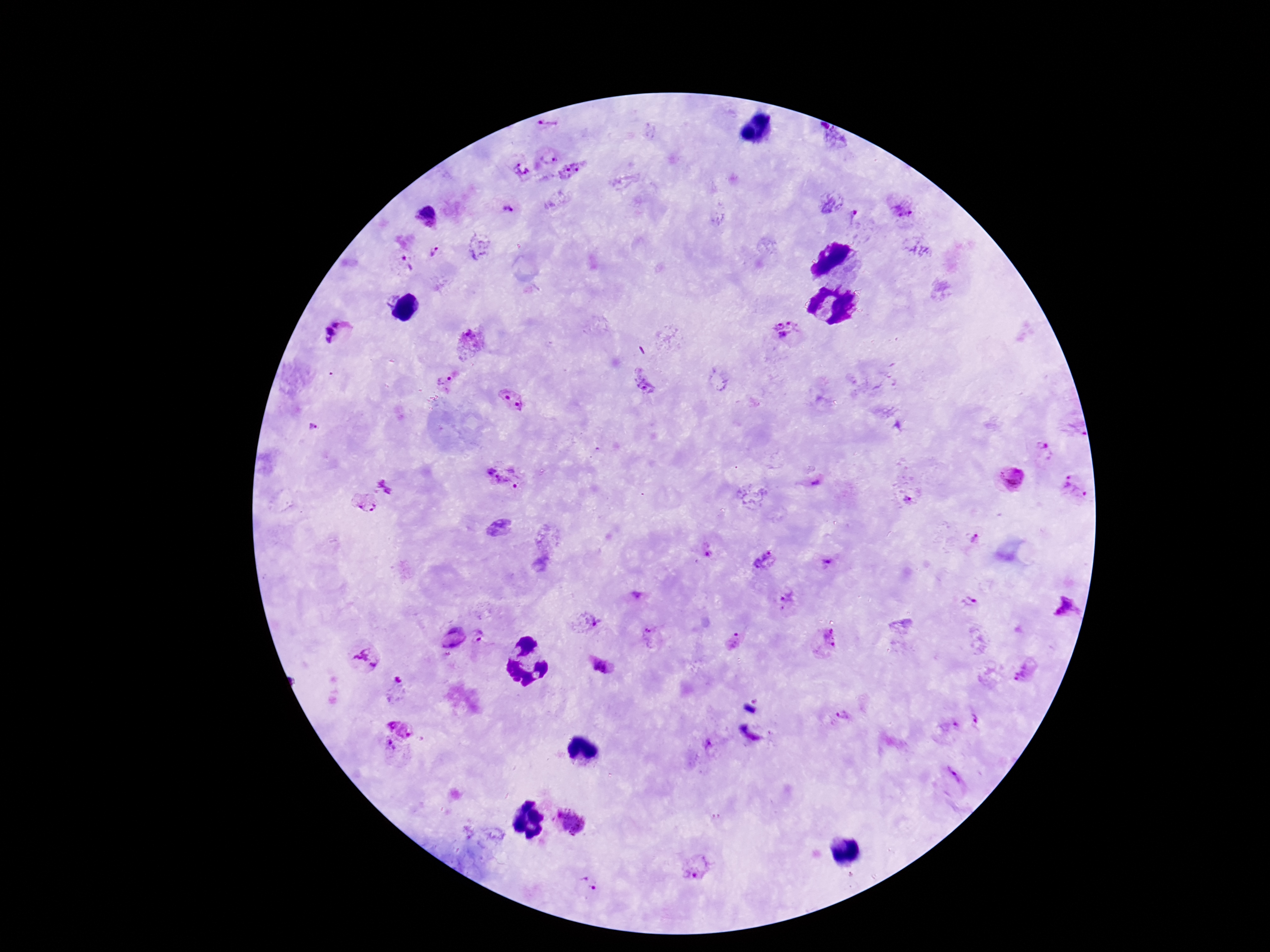

Approximate centers as {x, y} in pixels. Plasmodium parasite locations: {548, 124}, {829, 135}, {548, 157}, {523, 168}, {573, 171}, {901, 206}, {508, 210}, {426, 215}, {856, 218}, {478, 247}, {434, 252}, {405, 264}, {786, 331}, {339, 332}, {470, 343}, {444, 381}, {642, 381}, {512, 400}, {1041, 449}, {1012, 478}, {502, 479}, {815, 482}, {389, 484}, {1074, 487}, {905, 498}, {362, 502}, {970, 537}, {708, 554}, {764, 558}, {826, 561}, {787, 598}, {969, 603}, {1066, 609}, {585, 621}, {651, 636}, {453, 638}, {480, 639}, {825, 640}, {735, 643}, {364, 659}, {605, 667}, {1027, 670}, {397, 686}, {841, 715}, {979, 720}, {402, 728}, {947, 728}, {390, 747}, {952, 777}, {570, 821}, {695, 864}, {588, 885}. One field from this slide. Giemsa-stained preparation. Image is 1270×952 pixels. 100x magnification. Patient malaria status: infected. Thick blood film. Photographed through the microscope eyepiece with a smartphone camera.